Identify the parasite.
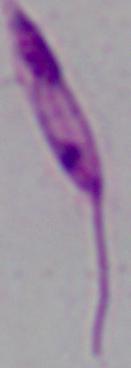
Leishmania.

Photomicrograph. Captured at 1000x magnification.